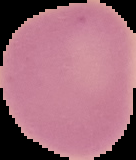

From a thin blood smear. Image is 136×160 pixels. Malaria status: uninfected. Cell region segmented out of the field of view; the surrounding area is masked to black.